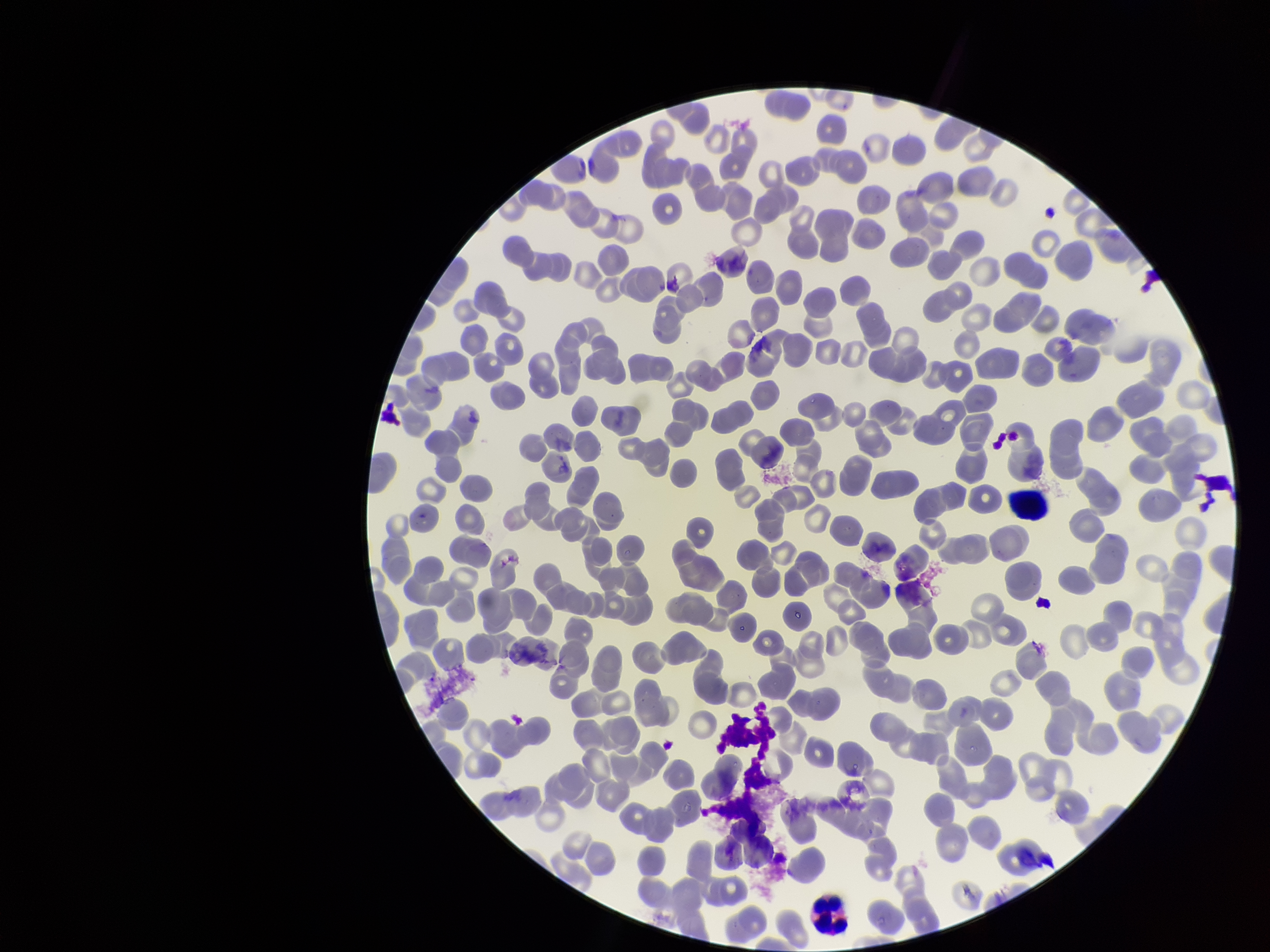

Giemsa stain. Image is 1270×952 pixels. Smartphone photograph taken through the eyepiece of a microscope. Parasitized red blood cell count: 0. Red blood cell count: 272. One field from this slide. Patient malaria status: negative. Parasitized red blood cells: none seen. Preparation: thin.